Locate every blood parasite and identify its species.
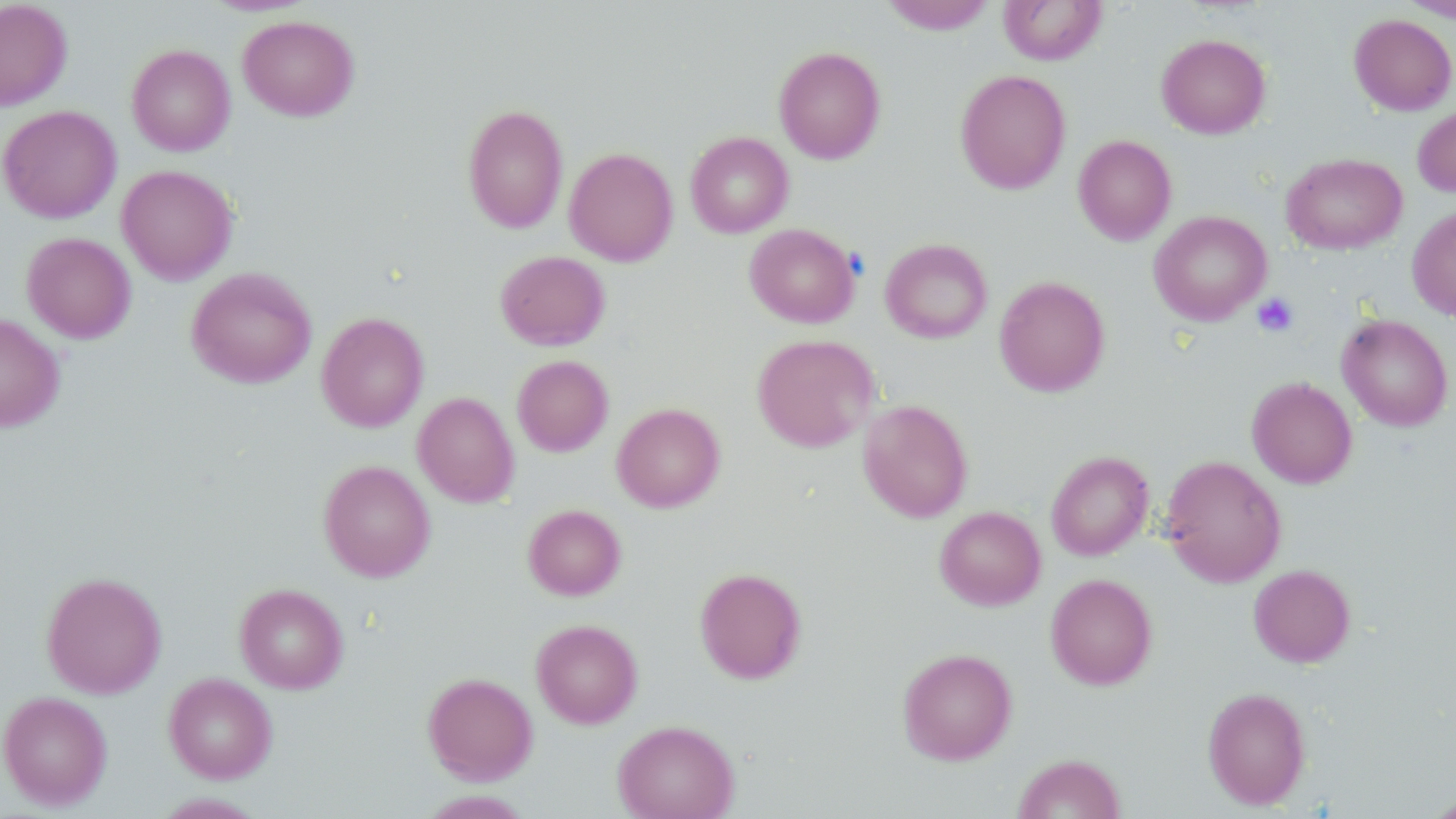
No blood parasites seen.

Summary:
  - Coordinate format: approximate bounding boxes as named x1/y1/x2/y2 corners in pixels
  - Uninfected red blood cell locations: (x1=0, y1=0, x2=72, y2=111), (x1=199, y1=0, x2=319, y2=16), (x1=880, y1=0, x2=997, y2=34), (x1=998, y1=0, x2=1107, y2=65), (x1=1400, y1=0, x2=1456, y2=21), (x1=1349, y1=14, x2=1456, y2=115), (x1=238, y1=15, x2=359, y2=121), (x1=1156, y1=33, x2=1271, y2=139), (x1=126, y1=44, x2=235, y2=156), (x1=773, y1=46, x2=886, y2=164), (x1=955, y1=69, x2=1071, y2=194), (x1=462, y1=103, x2=569, y2=234), (x1=1413, y1=103, x2=1456, y2=197), (x1=0, y1=105, x2=122, y2=223), (x1=686, y1=131, x2=794, y2=238), (x1=1073, y1=135, x2=1177, y2=245), (x1=564, y1=147, x2=678, y2=266), (x1=1281, y1=152, x2=1407, y2=254), (x1=117, y1=164, x2=238, y2=284), (x1=1407, y1=205, x2=1456, y2=322), (x1=1148, y1=210, x2=1271, y2=325), (x1=744, y1=223, x2=860, y2=328), (x1=21, y1=232, x2=136, y2=343), (x1=880, y1=238, x2=992, y2=343), (x1=495, y1=250, x2=610, y2=350), (x1=185, y1=267, x2=317, y2=388), (x1=993, y1=275, x2=1110, y2=397), (x1=316, y1=311, x2=429, y2=432), (x1=0, y1=313, x2=66, y2=432), (x1=1337, y1=313, x2=1453, y2=431), (x1=751, y1=334, x2=879, y2=452), (x1=512, y1=355, x2=613, y2=456), (x1=1246, y1=376, x2=1358, y2=489), (x1=413, y1=391, x2=519, y2=507), (x1=858, y1=399, x2=973, y2=522), (x1=611, y1=402, x2=726, y2=512), (x1=1046, y1=450, x2=1153, y2=560), (x1=1161, y1=455, x2=1287, y2=587), (x1=318, y1=459, x2=436, y2=582), (x1=523, y1=504, x2=626, y2=600), (x1=935, y1=506, x2=1046, y2=610), (x1=1249, y1=564, x2=1356, y2=667), (x1=694, y1=567, x2=807, y2=683), (x1=41, y1=571, x2=167, y2=698), (x1=1045, y1=573, x2=1158, y2=689), (x1=234, y1=583, x2=348, y2=694), (x1=531, y1=619, x2=643, y2=728), (x1=897, y1=647, x2=1017, y2=765), (x1=164, y1=672, x2=278, y2=783), (x1=422, y1=672, x2=538, y2=784), (x1=1202, y1=686, x2=1311, y2=809), (x1=0, y1=690, x2=113, y2=810), (x1=613, y1=719, x2=739, y2=819), (x1=1013, y1=753, x2=1126, y2=818), (x1=416, y1=790, x2=534, y2=818), (x1=1422, y1=792, x2=1456, y2=818)
  - Platelet locations: (x1=1252, y1=293, x2=1299, y2=337)
  - Slide-level diagnosis: negative for blood parasites
  - Stain: May-Grünwald-Giemsa
  - Modality: light microscopy
  - Preparation: thin blood film
  - Field of view: single
  - Magnification: 1000x
  - Image size: 1456×819 pixels